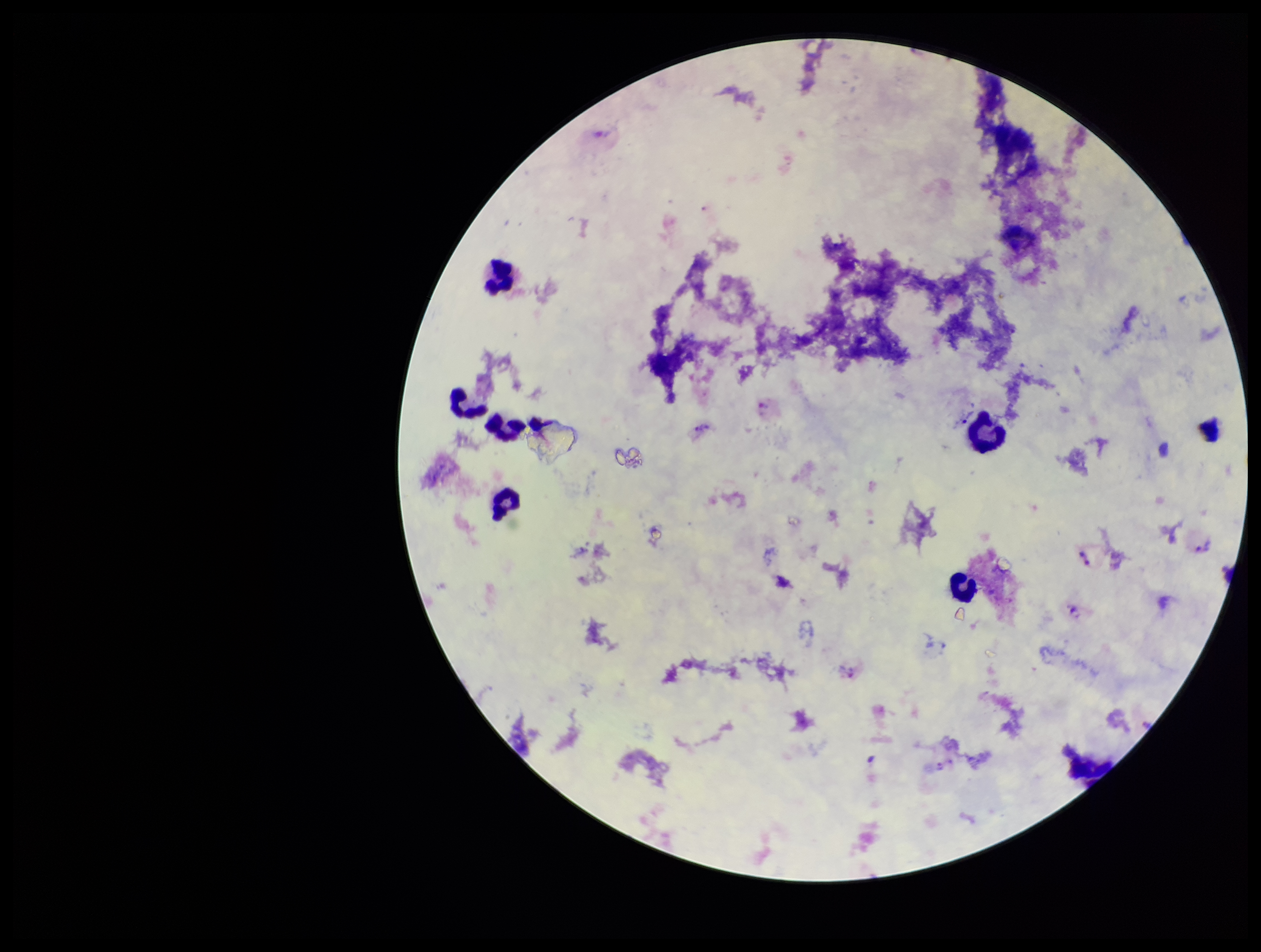
Summary:
  - Species reported for this patient: Plasmodium vivax
  - Stain: Giemsa
  - Leukocyte count: 6
  - Patient malaria status: positive
  - Field of view: single
  - Plasmodium parasites: detected
  - Preparation: thick smear
  - Capture: smartphone photograph through the microscope eyepiece
  - Parasite count: 6
  - Image size: 1261×952 pixels